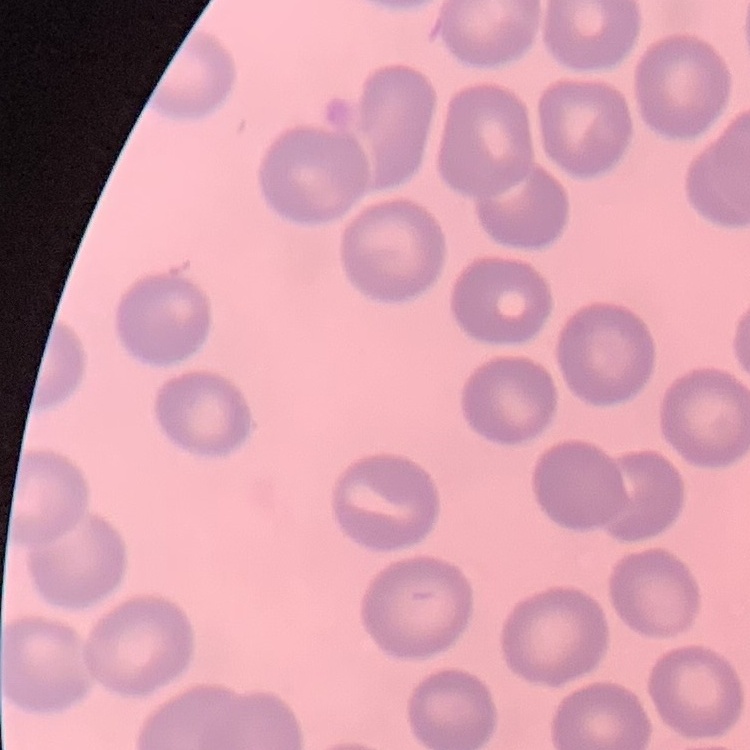
erythrocyte morphology = no rouleaux formation
image type = one tile cut from a larger photomicrograph
stain = Field's or Giemsa
preparation = thin blood smear